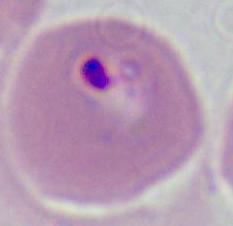

identification: Plasmodium
magnification: 400x or 1000x
modality: micrograph